Identify the parasite.
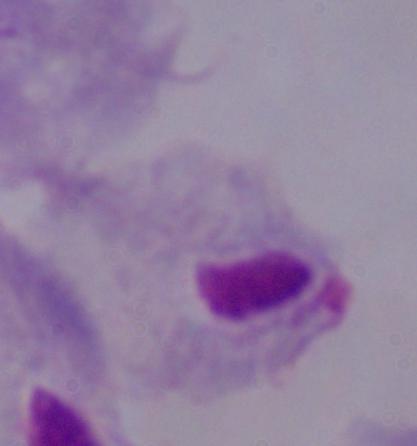

This is a trichomonad.

Summary:
  - Magnification: 1000x
  - Modality: photomicrograph